Name the cell type shown.
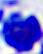
A leukocyte.

Summary:
  - Modality: photomicrograph
  - Magnification: 400x